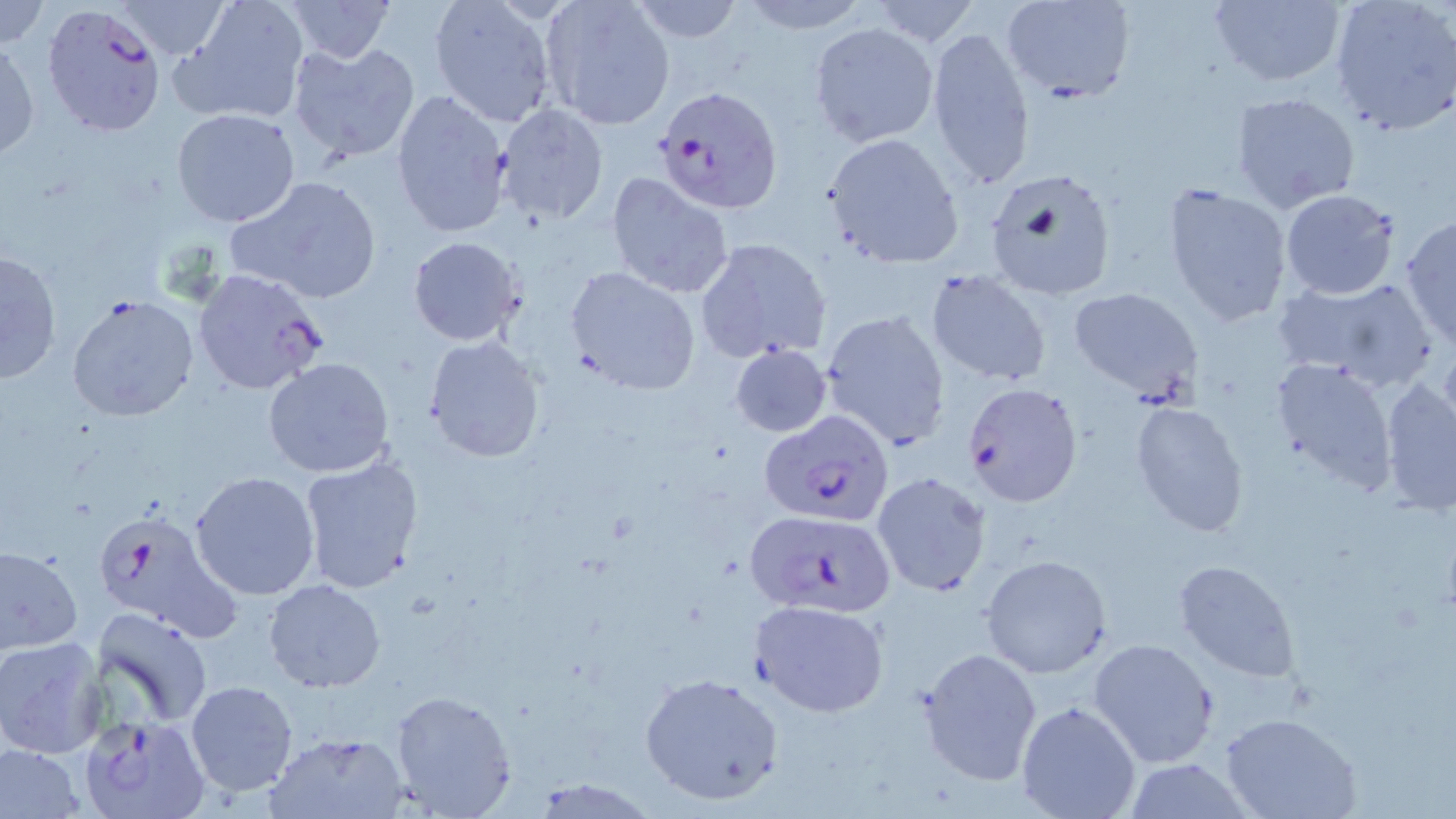

slide-level diagnosis = Plasmodium falciparum
magnification = 1000x
modality = optical microscopy
field of view = one of a larger specimen
image size = 1456×819 pixels
Plasmodium falciparum-infected red blood cell locations = approximate bounding boxes as (x1,y1)-(x2,y2) corner pairs in pixels: (40,2)-(168,139), (657,89)-(782,212), (191,267)-(329,395), (960,381)-(1084,508), (760,410)-(895,524), (92,507)-(241,643), (744,509)-(898,619), (82,712)-(211,819)
preparation = thin blood film
stain = May-Grünwald-Giemsa
uninfected red blood cell locations = approximate bounding boxes as (x1,y1)-(x2,y2) corner pairs in pixels: (0,0)-(47,49), (171,0)-(310,126), (281,0)-(396,65), (428,0)-(556,126), (537,0)-(674,130), (626,0)-(746,43), (735,0)-(871,32), (867,0)-(982,45), (1000,0)-(1134,105), (1208,0)-(1347,88), (1330,0)-(1456,135), (110,1)-(236,61), (808,21)-(936,146), (925,25)-(1036,196), (1,36)-(40,163), (287,40)-(423,162), (391,88)-(513,237), (1229,91)-(1361,213), (494,103)-(609,227), (172,108)-(301,227), (824,133)-(963,267), (982,168)-(1118,300), (606,171)-(735,298), (225,175)-(383,306), (1162,182)-(1292,329), (1279,189)-(1400,299), (1400,215)-(1456,347), (408,235)-(524,346), (695,237)-(834,364), (1,247)-(63,386), (566,267)-(702,395), (926,269)-(1053,387), (1272,276)-(1441,393), (1068,286)-(1205,401), (65,294)-(199,423), (820,310)-(951,450), (424,336)-(546,463), (729,343)-(833,438), (1268,356)-(1399,492), (263,357)-(398,480), (1378,376)-(1456,516), (1128,400)-(1249,537), (297,456)-(424,597), (189,471)-(322,600), (872,472)-(991,597), (0,544)-(83,654), (980,554)-(1112,676), (1173,559)-(1299,683), (263,580)-(385,693), (751,600)-(890,717), (93,607)-(213,728), (0,636)-(111,758), (1089,637)-(1219,769), (918,648)-(1041,786), (640,671)-(786,807), (185,680)-(298,798), (390,690)-(516,818), (1015,700)-(1142,819), (1222,713)-(1361,819), (265,730)-(407,818), (0,742)-(87,818), (1120,759)-(1255,817), (527,778)-(658,816)